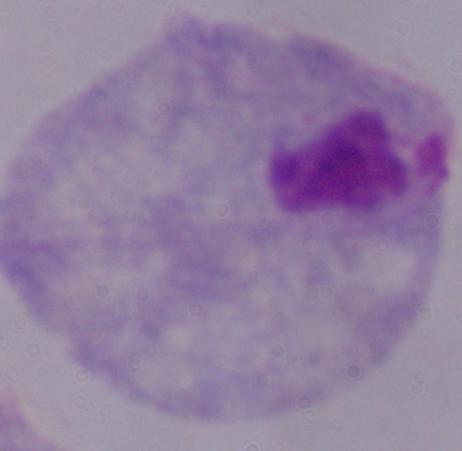
modality: micrograph
magnification: 1000x
identification: trichomonad